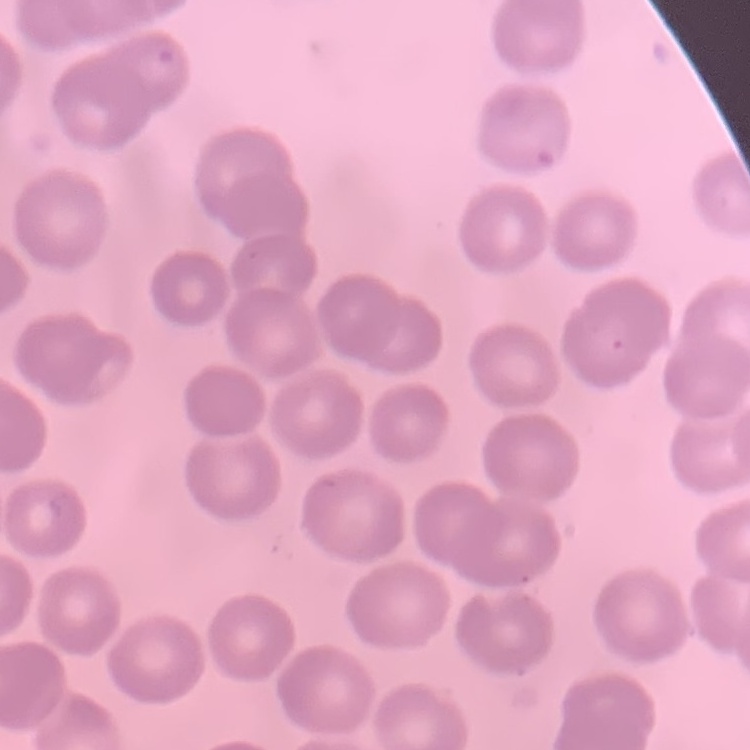
Summary:
  - Red blood cell morphology: no rouleaux formation
  - Preparation: thin blood film
  - Image type: one tile cut from a larger photomicrograph
  - Stain: Field's or Giemsa